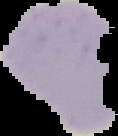
Malaria status: parasitized. Segmented cell region on a black background. Image is 118×136 pixels. From a thin blood film.